Locate every blood parasite and identify its species.
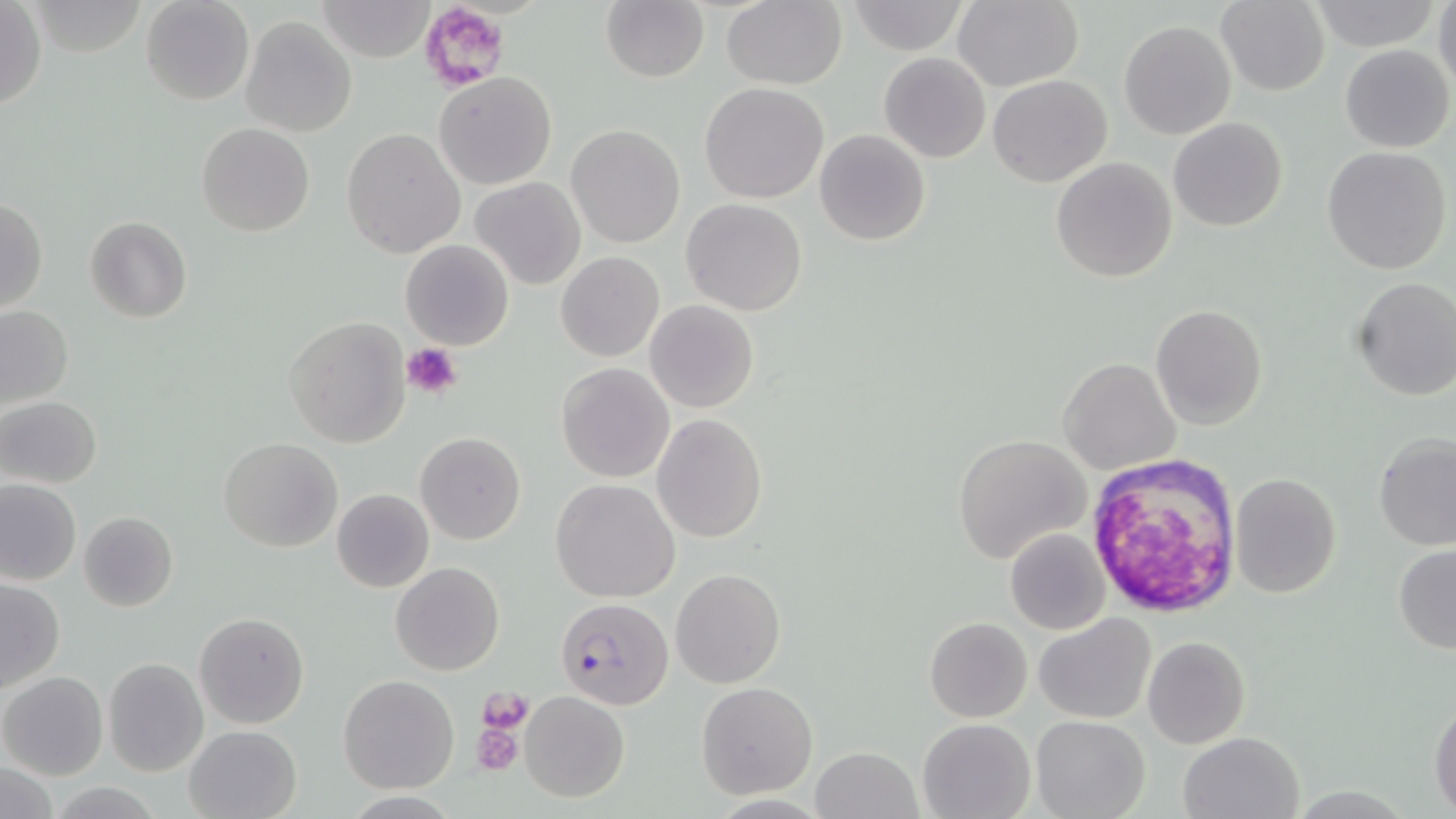
Approximate bounding boxes as named x1/y1/x2/y2 corners in pixels.
Plasmodium falciparum-infected red blood cells: (x1=554, y1=598, x2=672, y2=709).
No Plasmodium ovale, Plasmodium malariae, Plasmodium vivax, Babesia divergens, or Trypanosoma brucei observed.

Summary:
  - Uninfected red blood cell locations: (x1=139, y1=0, x2=254, y2=106), (x1=316, y1=0, x2=436, y2=63), (x1=600, y1=0, x2=709, y2=83), (x1=1433, y1=0, x2=1456, y2=94), (x1=721, y1=1, x2=846, y2=89), (x1=951, y1=1, x2=1083, y2=91), (x1=1215, y1=1, x2=1330, y2=95), (x1=1308, y1=1, x2=1437, y2=49), (x1=0, y1=2, x2=45, y2=109), (x1=846, y1=2, x2=971, y2=54), (x1=241, y1=15, x2=357, y2=136), (x1=1119, y1=20, x2=1235, y2=139), (x1=1339, y1=44, x2=1453, y2=152), (x1=879, y1=52, x2=990, y2=163), (x1=434, y1=72, x2=558, y2=191), (x1=987, y1=73, x2=1112, y2=186), (x1=700, y1=82, x2=829, y2=204), (x1=1169, y1=117, x2=1288, y2=233), (x1=197, y1=122, x2=314, y2=236), (x1=567, y1=125, x2=686, y2=248), (x1=341, y1=129, x2=466, y2=258), (x1=814, y1=129, x2=930, y2=246), (x1=1322, y1=147, x2=1451, y2=276), (x1=1051, y1=156, x2=1178, y2=282), (x1=469, y1=176, x2=585, y2=291), (x1=1, y1=197, x2=47, y2=312), (x1=681, y1=199, x2=808, y2=316), (x1=85, y1=217, x2=193, y2=322), (x1=400, y1=240, x2=515, y2=351), (x1=556, y1=251, x2=664, y2=361), (x1=1350, y1=277, x2=1456, y2=401), (x1=645, y1=301, x2=759, y2=414), (x1=0, y1=305, x2=74, y2=413), (x1=1151, y1=305, x2=1268, y2=429), (x1=284, y1=316, x2=411, y2=448), (x1=1057, y1=357, x2=1181, y2=474), (x1=557, y1=363, x2=674, y2=482), (x1=1, y1=397, x2=102, y2=489), (x1=651, y1=414, x2=768, y2=543), (x1=415, y1=431, x2=525, y2=545), (x1=1374, y1=432, x2=1455, y2=551), (x1=952, y1=434, x2=1092, y2=563), (x1=218, y1=437, x2=342, y2=552), (x1=1229, y1=472, x2=1341, y2=597), (x1=1, y1=479, x2=80, y2=585), (x1=551, y1=479, x2=680, y2=602), (x1=331, y1=488, x2=435, y2=593), (x1=79, y1=511, x2=178, y2=612), (x1=1005, y1=526, x2=1111, y2=635), (x1=1393, y1=546, x2=1456, y2=654), (x1=391, y1=561, x2=504, y2=675), (x1=671, y1=568, x2=785, y2=687), (x1=0, y1=578, x2=65, y2=693), (x1=194, y1=611, x2=309, y2=729), (x1=1035, y1=612, x2=1157, y2=724), (x1=923, y1=615, x2=1033, y2=723), (x1=1142, y1=636, x2=1251, y2=749), (x1=103, y1=657, x2=209, y2=776), (x1=0, y1=671, x2=109, y2=780), (x1=338, y1=675, x2=458, y2=793), (x1=697, y1=682, x2=818, y2=799), (x1=521, y1=692, x2=628, y2=802), (x1=1429, y1=699, x2=1456, y2=814), (x1=1031, y1=715, x2=1149, y2=819), (x1=917, y1=717, x2=1037, y2=819), (x1=183, y1=724, x2=301, y2=818), (x1=1178, y1=730, x2=1306, y2=819), (x1=811, y1=747, x2=920, y2=819), (x1=1, y1=761, x2=58, y2=818), (x1=47, y1=781, x2=167, y2=817)
  - Platelet locations: (x1=417, y1=2, x2=511, y2=91), (x1=403, y1=342, x2=463, y2=399), (x1=1083, y1=454, x2=1242, y2=617), (x1=480, y1=687, x2=533, y2=734), (x1=473, y1=719, x2=524, y2=776)
  - Slide-level diagnosis: Plasmodium falciparum
  - Stain: May-Grünwald-Giemsa
  - Magnification: 1000x
  - Image size: 1456×819 pixels
  - Field of view: single
  - Modality: light microscopy
  - Preparation: thin blood smear